Locate every uninfected red blood cell.
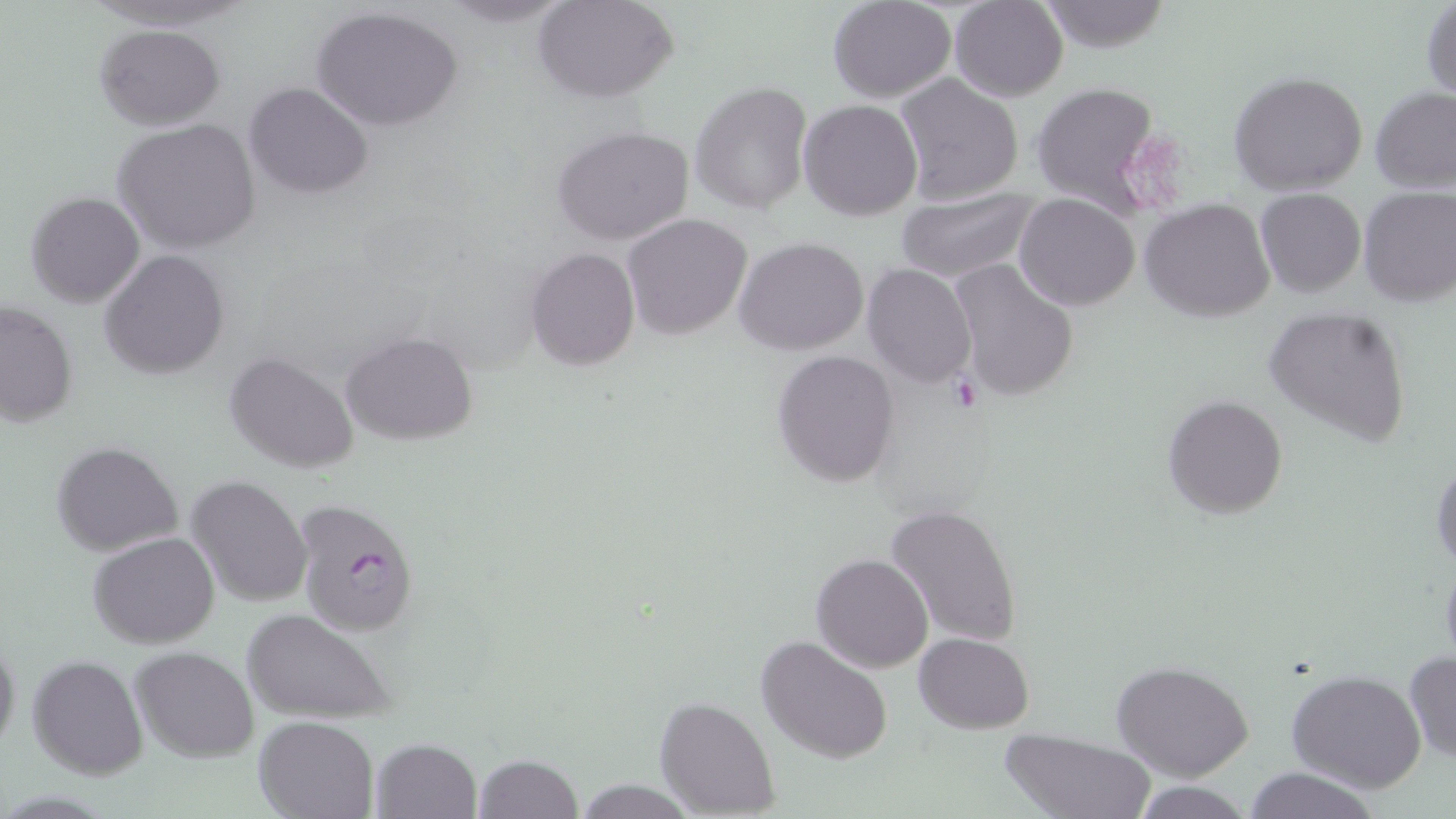
Approximate bounding boxes as (x1, y1, x2, y2) in pixels.
Uninfected red blood cells: (433, 0, 577, 27), (535, 0, 679, 103), (829, 0, 957, 102), (949, 0, 1069, 101), (1036, 0, 1174, 52), (1421, 2, 1455, 102), (312, 5, 464, 133), (95, 25, 223, 129), (1228, 70, 1368, 194), (894, 74, 1022, 207), (691, 82, 812, 216), (1027, 82, 1164, 212), (245, 83, 371, 199), (1369, 89, 1456, 193), (799, 98, 923, 221), (114, 117, 262, 254), (552, 126, 695, 247), (1357, 185, 1455, 306), (893, 188, 1039, 282), (1255, 188, 1366, 298), (25, 191, 145, 308), (1015, 193, 1140, 311), (1141, 199, 1277, 321), (622, 214, 751, 339), (734, 237, 869, 356), (526, 247, 639, 372), (100, 249, 229, 380), (947, 260, 1079, 403), (863, 262, 976, 387), (1, 301, 78, 428), (1262, 307, 1413, 446), (341, 333, 479, 443), (771, 349, 897, 487), (225, 350, 360, 473), (1161, 394, 1289, 520), (51, 441, 184, 554), (1432, 456, 1456, 573), (186, 475, 313, 607), (883, 505, 1023, 648), (88, 531, 222, 647), (811, 552, 933, 673), (1439, 554, 1456, 670), (241, 608, 397, 725), (914, 632, 1034, 733), (0, 634, 21, 757), (756, 634, 894, 764), (130, 645, 259, 762), (1404, 651, 1456, 765), (27, 654, 148, 779), (1110, 660, 1253, 782), (1286, 671, 1426, 793), (655, 697, 780, 816), (253, 717, 379, 819), (998, 726, 1156, 819), (370, 738, 481, 819), (472, 753, 583, 819), (1242, 767, 1383, 819), (572, 779, 698, 816), (1130, 782, 1257, 818).

slide-level diagnosis = Plasmodium falciparum
stain = May-Grünwald-Giemsa
field of view = single
image size = 1456×819 pixels
modality = optical microscopy
magnification = 1000x
Plasmodium falciparum-infected red blood cell locations = approximate bounding boxes as (x1, y1, x2, y2) in pixels: (291, 496, 420, 638)
preparation = thin blood smear
platelet locations = approximate bounding boxes as (x1, y1, x2, y2) in pixels: (1127, 141, 1181, 209)